Outline each blood parasite and name the species.
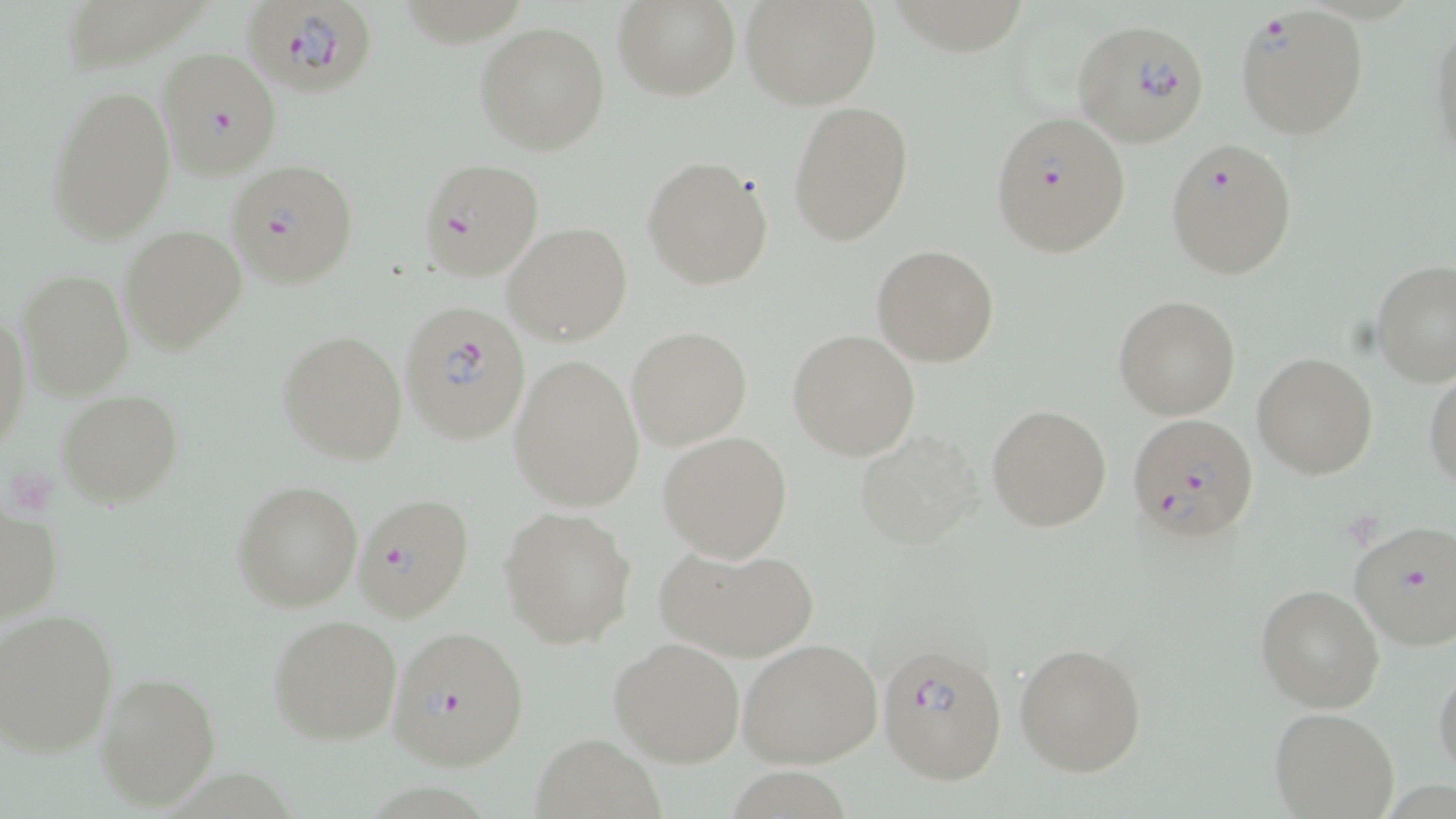

Approximate bounding boxes as (x1,y1)-(x2,y2) corner pairs in pixels.
Plasmodium falciparum-infected red blood cells: (244,0)-(380,97), (1232,5)-(1371,141), (1071,19)-(1210,147), (156,46)-(283,179), (990,110)-(1131,258), (1163,138)-(1297,280), (418,158)-(545,282), (227,160)-(358,289), (395,300)-(538,448), (1125,413)-(1258,542), (353,491)-(476,622), (1348,519)-(1456,651), (388,624)-(530,770), (875,640)-(1008,785).
No Plasmodium ovale, Plasmodium malariae, Plasmodium vivax, Babesia divergens, or Trypanosoma brucei observed.

Platelet locations: (15,472)-(56,517). Uninfected red blood cell locations: (616,0)-(740,99), (742,0)-(882,110), (1428,12)-(1456,168), (476,21)-(611,157), (46,81)-(175,246), (788,100)-(912,247), (643,154)-(774,290), (504,222)-(631,346), (119,225)-(246,356), (872,244)-(999,367), (1371,260)-(1456,386), (16,270)-(134,400), (1114,295)-(1241,419), (0,309)-(31,451), (626,325)-(752,449), (278,328)-(407,465), (788,329)-(921,459), (1252,352)-(1378,478), (508,355)-(645,511), (1424,369)-(1456,490), (55,390)-(184,509), (987,404)-(1112,532), (852,429)-(985,552), (657,431)-(793,561), (233,479)-(363,612), (0,504)-(64,627), (499,506)-(637,649), (652,540)-(820,662), (1255,585)-(1384,713), (0,607)-(120,758), (268,614)-(401,743), (610,637)-(745,768), (738,637)-(884,770), (1013,641)-(1146,777), (1433,662)-(1456,783), (95,671)-(222,809), (1268,707)-(1399,818), (528,735)-(663,818). Slide-level diagnosis: Plasmodium falciparum. Single field of view. Optical microscopy. 1000x magnification. Image is 1456×819 pixels. Thin blood film. May-Grünwald-Giemsa stain.